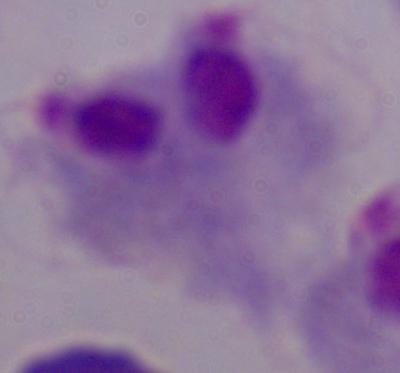

Captured at 1000x magnification. A trichomonad is seen. Micrograph.